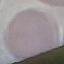

Summary:
  - Result: negative for malaria parasites
  - Preparation: thin blood smear
  - Stain: Giemsa
  - Image type: cell patch, automatically extracted from a larger field of view and resized to 64 × 64 pixels
  - Capture: smartphone through the microscope eyepiece